Outline each blood parasite and name the species.
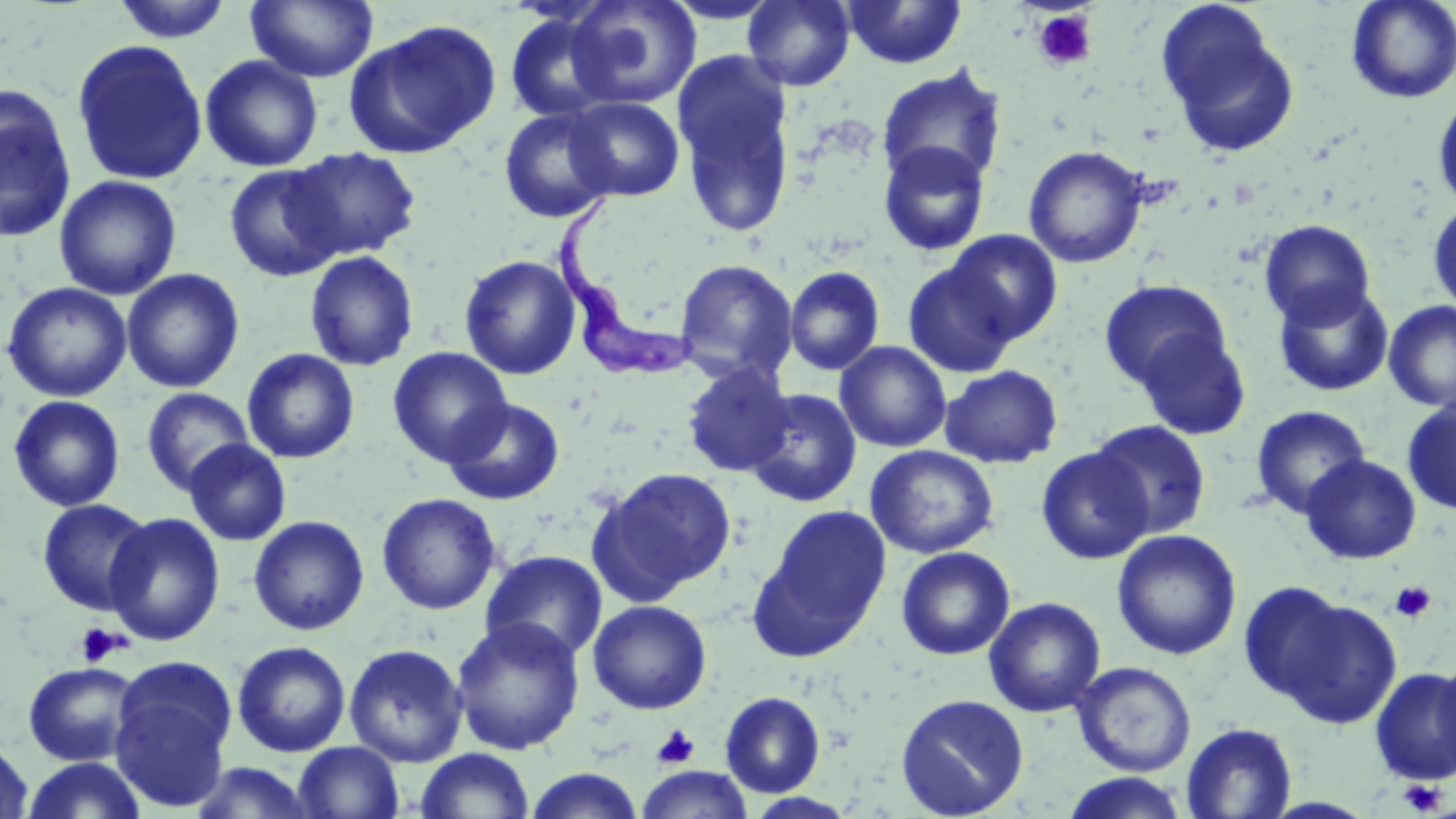

Approximate bounding boxes as (x1,y1)-(x2,y2) corner pairs in pixels.
Trypanosoma brucei: (555,191)-(699,383).
No Plasmodium falciparum, Plasmodium ovale, Plasmodium malariae, Plasmodium vivax, or Babesia divergens observed.

Uninfected red blood cell locations: (111,0)-(234,43), (245,0)-(379,83), (742,0)-(856,91), (841,0)-(967,69), (1346,0)-(1456,103), (565,1)-(701,109), (1155,3)-(1299,157), (504,10)-(619,125), (345,19)-(502,158), (70,38)-(208,187), (673,51)-(798,238), (200,55)-(323,172), (876,65)-(1008,190), (0,87)-(78,244), (1433,92)-(1456,212), (564,96)-(685,201), (499,106)-(617,224), (878,141)-(990,256), (1023,144)-(1149,268), (285,147)-(421,262), (224,163)-(346,283), (54,175)-(182,300), (1428,200)-(1456,316), (1259,219)-(1376,328), (944,229)-(1063,345), (304,251)-(419,371), (460,254)-(581,380), (674,259)-(799,384), (902,259)-(1022,379), (784,266)-(885,376), (121,268)-(245,393), (1098,278)-(1233,395), (1,281)-(133,403), (1272,282)-(1395,397), (1383,301)-(1456,411), (1131,325)-(1252,440), (835,341)-(952,453), (387,347)-(513,467), (242,348)-(360,464), (680,363)-(795,478), (939,364)-(1063,468), (141,387)-(254,496), (745,388)-(862,508), (8,395)-(126,511), (443,397)-(565,505), (1402,397)-(1456,515), (1250,405)-(1371,519), (1088,419)-(1211,539), (184,439)-(291,546), (865,445)-(999,559), (1036,446)-(1153,564), (1300,454)-(1422,564), (592,467)-(736,598), (376,492)-(501,615), (37,498)-(153,616), (751,507)-(891,658), (104,512)-(225,646), (248,515)-(370,636), (1112,529)-(1242,660), (896,546)-(1016,660), (481,549)-(608,663), (1238,581)-(1353,706), (1274,594)-(1404,729), (983,596)-(1106,717), (588,599)-(712,714), (450,616)-(586,755), (232,640)-(352,758), (344,643)-(468,767), (1434,653)-(1456,783), (109,659)-(238,813), (1072,661)-(1197,777), (23,662)-(140,766), (1369,666)-(1456,786), (720,691)-(825,797), (895,693)-(1029,818), (1180,722)-(1298,818), (0,736)-(35,818), (293,741)-(405,819), (414,748)-(535,818), (21,757)-(149,818), (188,761)-(320,819), (637,766)-(753,819), (523,767)-(645,818), (1060,772)-(1190,818). Platelet locations: (1032,9)-(1097,71), (1390,580)-(1436,624), (75,623)-(126,666), (652,724)-(700,770), (1397,779)-(1447,816). Slide-level diagnosis: Trypanosoma brucei. May-Grünwald-Giemsa stain. Thin blood smear. Image is 1456×819 pixels. One field of a larger specimen. Captured at 1000x magnification. Optical microscopy.